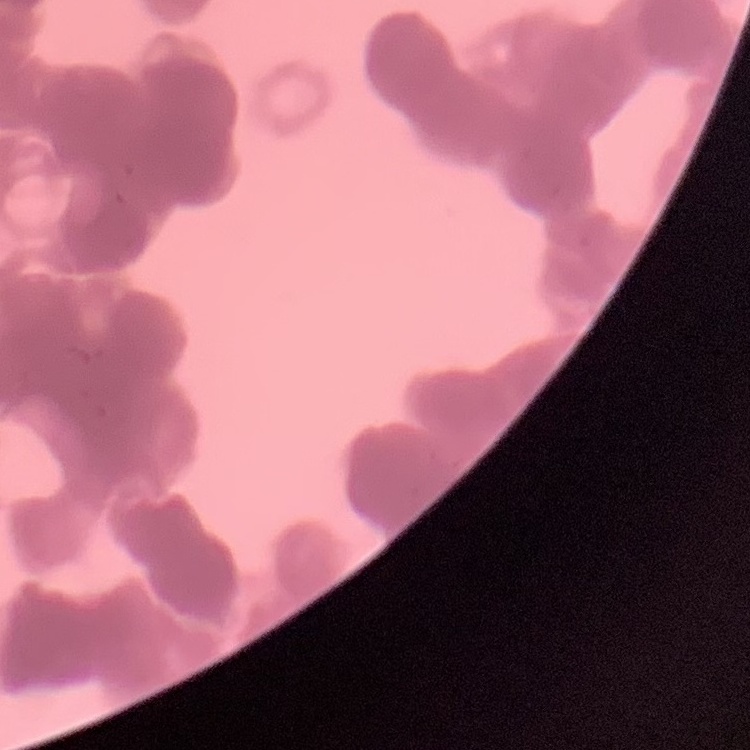

{
  "red_blood_cell_morphology": "rouleaux formation",
  "preparation": "thin blood film",
  "stain": "Field's or Giemsa",
  "image_type": "one tile cut from a larger photomicrograph"
}